Assess this cell for malaria.
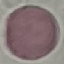

Uninfected.

Summary:
  - Capture: smartphone through the microscope eyepiece
  - Preparation: thin blood smear
  - Image type: automatically extracted cell patch, resized to 64 × 64 pixels
  - Stain: Giemsa